State the blood parasite species.
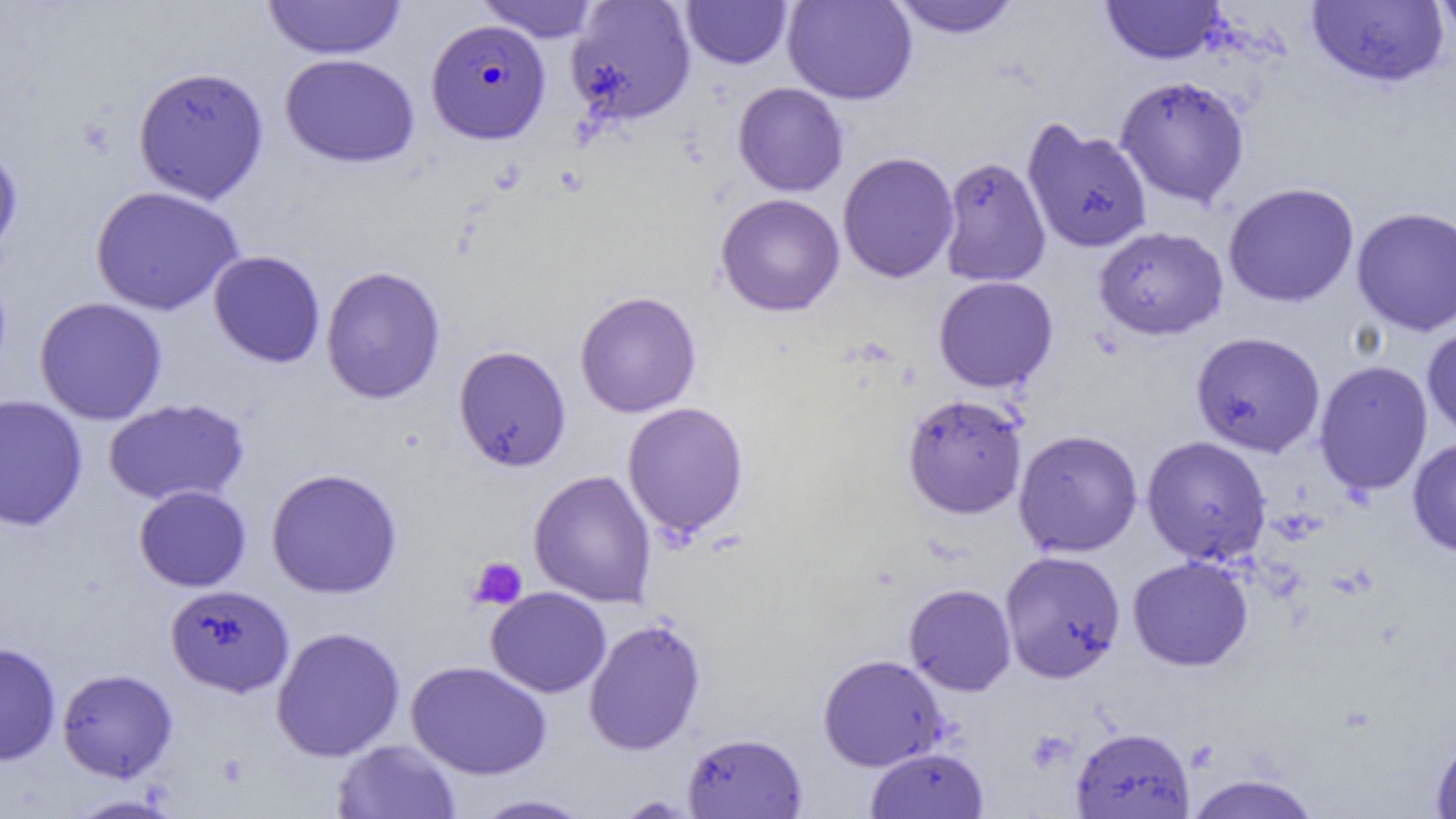
Plasmodium falciparum.

{
  "preparation": "thin blood smear",
  "plasmodium_falciparum_infected_red_blood_cell_locations": "approximate bounding boxes as [x1, y1, x2, y2] in pixels: [426, 19, 551, 143]",
  "uninfected_red_blood_cell_locations": "approximate bounding boxes as [x1, y1, x2, y2] in pixels: [474, 0, 603, 42], [682, 0, 792, 69], [782, 0, 917, 105], [889, 0, 1021, 39], [1307, 0, 1449, 88], [1432, 0, 1456, 44], [262, 1, 406, 59], [565, 1, 697, 126], [1100, 1, 1224, 65], [279, 53, 419, 168], [132, 65, 269, 204], [1114, 75, 1250, 208], [732, 82, 849, 197], [1023, 121, 1153, 254], [0, 140, 24, 269], [837, 152, 959, 283], [938, 156, 1051, 287], [1223, 182, 1360, 308], [90, 185, 244, 316], [715, 193, 845, 317], [1351, 206, 1456, 337], [1093, 226, 1229, 340], [208, 250, 326, 368], [320, 265, 446, 404], [933, 276, 1058, 393], [574, 290, 702, 418], [33, 296, 168, 425], [1422, 323, 1456, 442], [1190, 331, 1326, 457], [453, 345, 571, 472], [1314, 360, 1433, 496], [902, 393, 1027, 519], [0, 394, 88, 531], [102, 397, 250, 507], [621, 401, 750, 538], [1013, 428, 1143, 558], [1141, 435, 1272, 565], [1407, 437, 1456, 557], [265, 467, 403, 599], [528, 469, 656, 608], [133, 485, 251, 592], [999, 549, 1126, 683], [1127, 556, 1253, 671], [903, 583, 1016, 696], [165, 584, 295, 698], [485, 587, 611, 698], [583, 617, 707, 755], [270, 625, 405, 762], [0, 642, 61, 766], [817, 653, 948, 772], [405, 660, 552, 779], [56, 668, 178, 782], [1071, 726, 1195, 818], [681, 732, 808, 818], [1430, 732, 1456, 818], [331, 739, 461, 818], [865, 746, 989, 818], [1183, 773, 1323, 818], [470, 793, 595, 818], [66, 794, 186, 818], [613, 794, 703, 818]",
  "field_of_view": "one of a larger specimen",
  "platelet_locations": "approximate bounding boxes as [x1, y1, x2, y2] in pixels: [467, 556, 528, 611]",
  "magnification": "1000x",
  "modality": "light microscopy",
  "image_size": "1456×819 pixels"
}